Assess the morphology of the red blood cells.
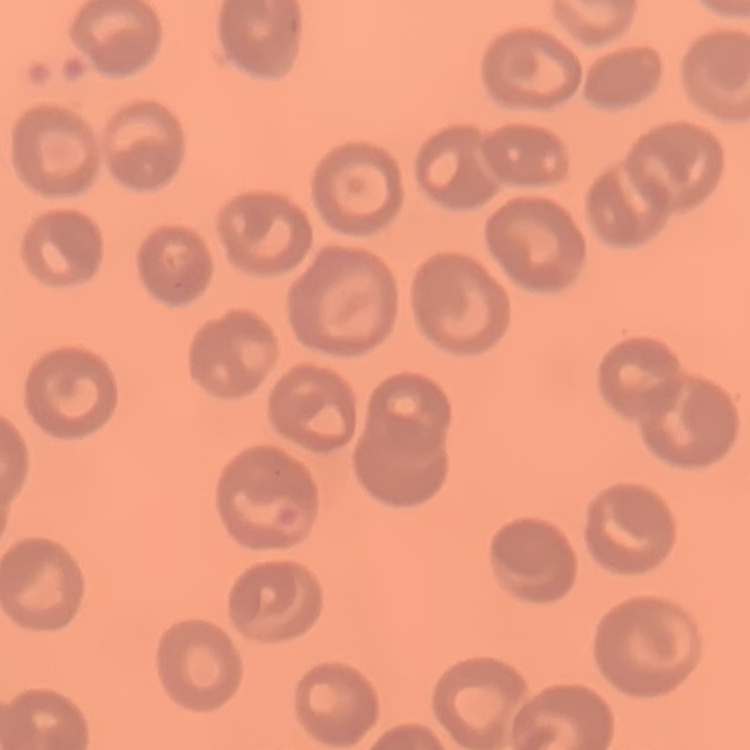
No rouleaux formation.

Stained with either Field's or Giemsa. One tile cut from a larger photomicrograph. Thin peripheral smear.